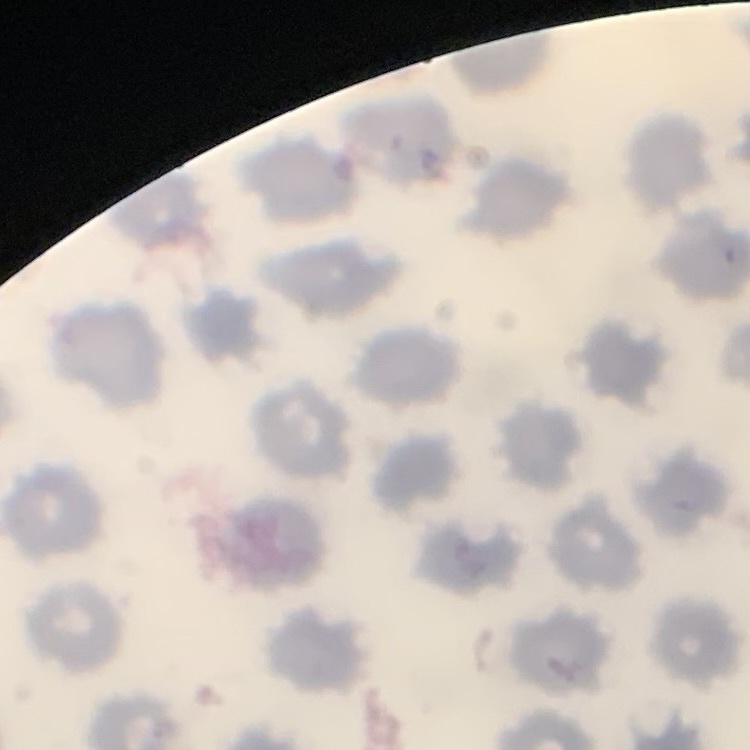
Summary:
  - Red blood cell morphology: no rouleaux formation
  - Stain: Field's or Giemsa
  - Image type: square crop of a larger photomicrograph
  - Preparation: thin blood film